Outline each uninfected red blood cell.
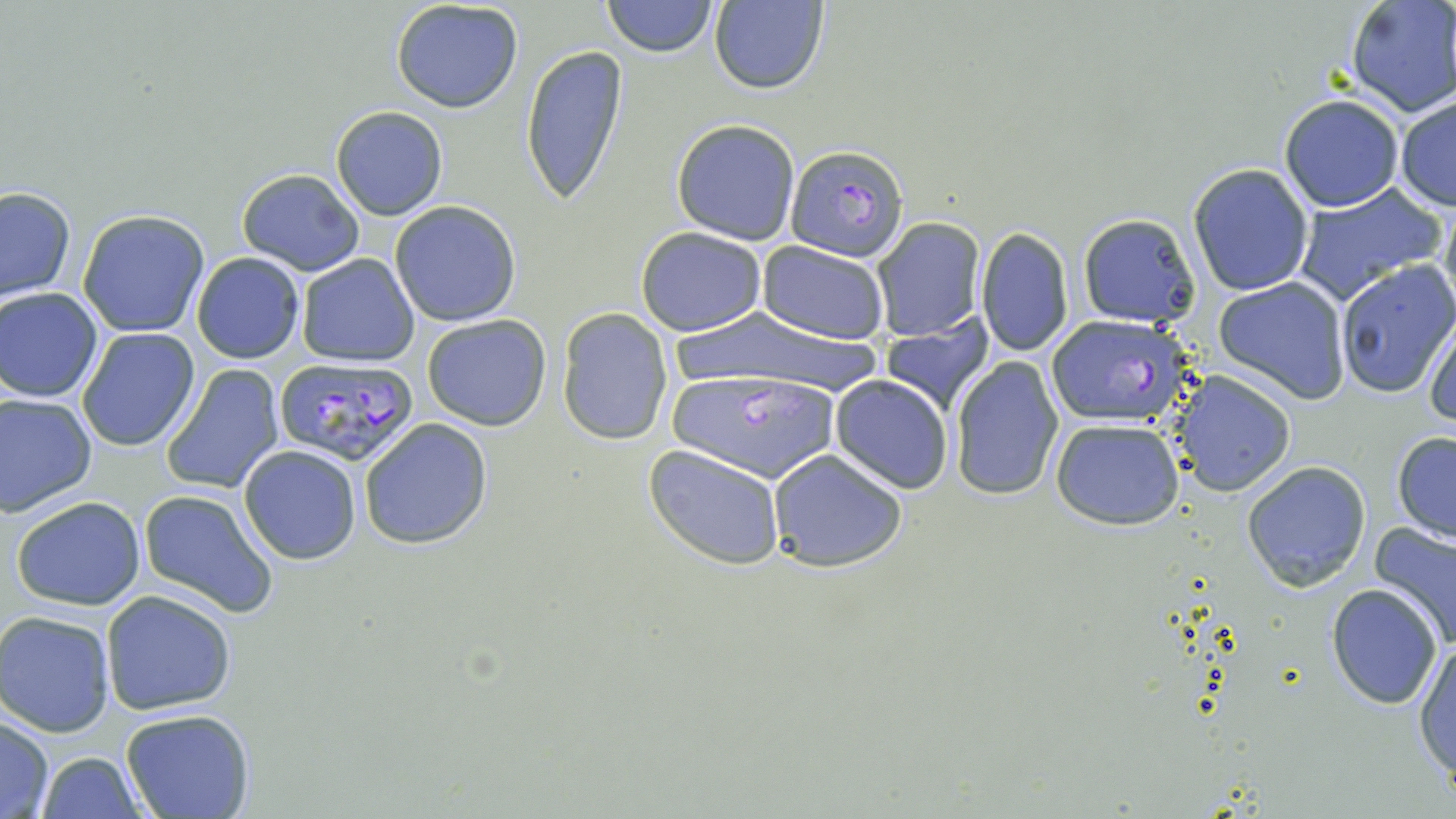

Approximate bounding boxes as named x1/y1/x2/y2 corners in pixels.
Uninfected red blood cells: (x1=602, y1=0, x2=717, y2=57), (x1=1344, y1=0, x2=1456, y2=120), (x1=389, y1=1, x2=524, y2=114), (x1=707, y1=1, x2=829, y2=95), (x1=520, y1=43, x2=629, y2=204), (x1=1279, y1=94, x2=1404, y2=212), (x1=1394, y1=95, x2=1456, y2=211), (x1=330, y1=106, x2=448, y2=221), (x1=671, y1=118, x2=801, y2=245), (x1=1188, y1=163, x2=1314, y2=296), (x1=236, y1=168, x2=365, y2=276), (x1=1290, y1=185, x2=1444, y2=304), (x1=1, y1=186, x2=76, y2=304), (x1=1437, y1=186, x2=1456, y2=323), (x1=390, y1=201, x2=521, y2=326), (x1=78, y1=209, x2=210, y2=337), (x1=1077, y1=212, x2=1201, y2=326), (x1=872, y1=218, x2=985, y2=342), (x1=634, y1=227, x2=767, y2=336), (x1=976, y1=227, x2=1074, y2=357), (x1=758, y1=242, x2=890, y2=345), (x1=192, y1=252, x2=305, y2=364), (x1=295, y1=255, x2=420, y2=367), (x1=1333, y1=260, x2=1455, y2=399), (x1=1212, y1=276, x2=1351, y2=403), (x1=1, y1=287, x2=105, y2=402), (x1=670, y1=306, x2=877, y2=395), (x1=556, y1=309, x2=674, y2=446), (x1=421, y1=315, x2=551, y2=429), (x1=882, y1=317, x2=995, y2=416), (x1=1422, y1=317, x2=1455, y2=429), (x1=77, y1=328, x2=201, y2=449), (x1=950, y1=359, x2=1066, y2=499), (x1=160, y1=364, x2=285, y2=494), (x1=1169, y1=370, x2=1297, y2=496), (x1=830, y1=375, x2=953, y2=494), (x1=0, y1=393, x2=97, y2=517), (x1=358, y1=418, x2=492, y2=550), (x1=1050, y1=418, x2=1185, y2=530), (x1=1391, y1=431, x2=1456, y2=542), (x1=238, y1=445, x2=363, y2=565), (x1=644, y1=446, x2=787, y2=568), (x1=767, y1=449, x2=910, y2=572), (x1=1241, y1=460, x2=1371, y2=590), (x1=138, y1=488, x2=279, y2=617), (x1=10, y1=494, x2=147, y2=611), (x1=1369, y1=522, x2=1456, y2=651), (x1=1327, y1=584, x2=1444, y2=709), (x1=100, y1=590, x2=238, y2=715), (x1=1, y1=611, x2=119, y2=736), (x1=1414, y1=637, x2=1456, y2=784), (x1=120, y1=709, x2=257, y2=819), (x1=0, y1=714, x2=55, y2=818), (x1=35, y1=750, x2=147, y2=819).

Plasmodium falciparum-infected red blood cell locations: (x1=784, y1=142, x2=910, y2=263), (x1=1045, y1=317, x2=1194, y2=426), (x1=273, y1=357, x2=421, y2=468), (x1=665, y1=369, x2=842, y2=479). Slide-level diagnosis: Plasmodium falciparum. One field of a larger specimen. Thin blood smear. Image is 1456×819 pixels. Light microscopy. 1000x magnification. May-Grünwald-Giemsa stain.